Outline platelets.
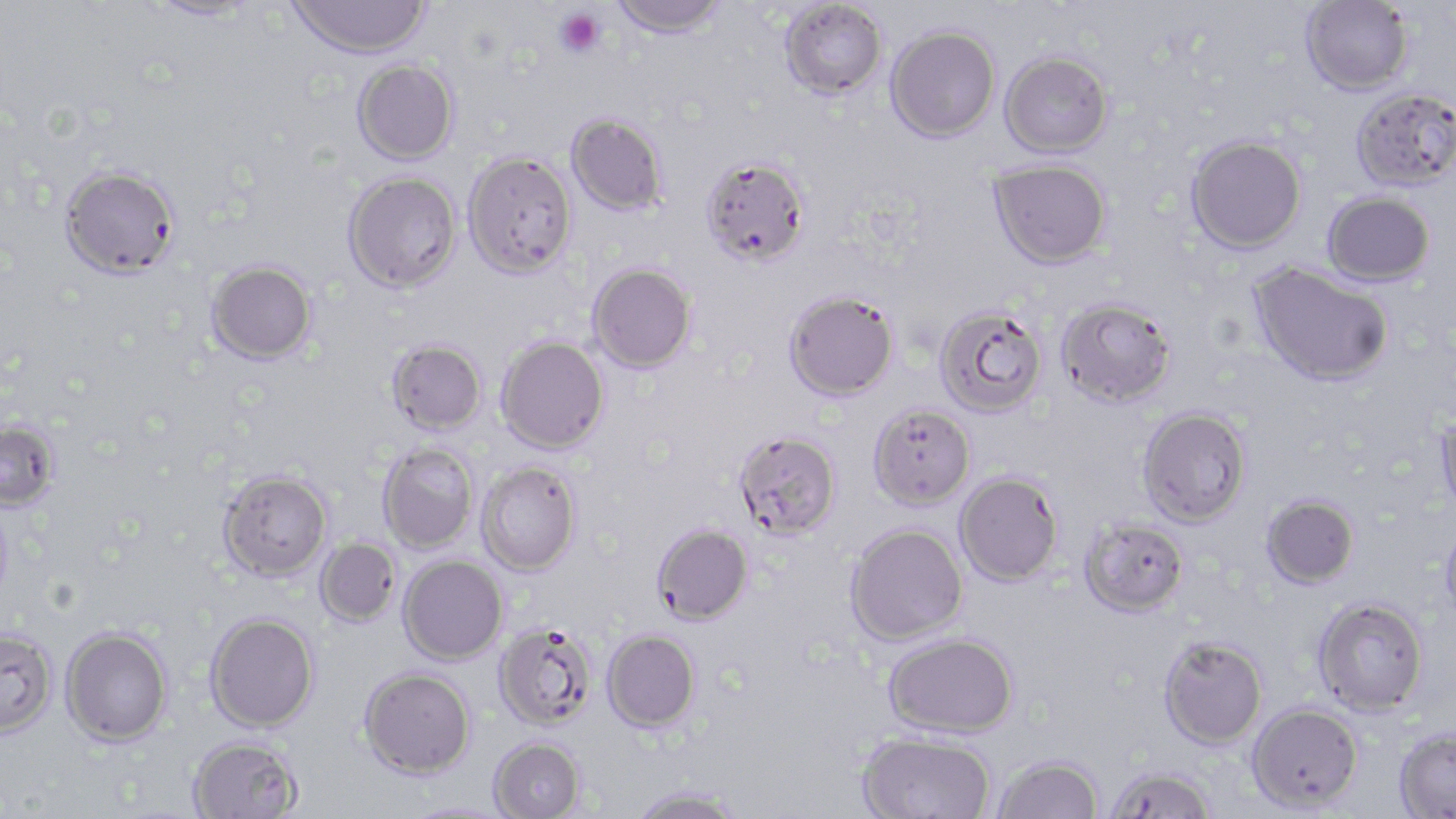

Approximate bounding boxes as [x1, y1, x2, y2] in pixels.
Platelets: [555, 7, 605, 58].

slide-level diagnosis = Plasmodium falciparum
stain = May-Grünwald-Giemsa
uninfected red blood cell locations = approximate bounding boxes as [x1, y1, x2, y2] in pixels: [288, 0, 430, 60], [608, 0, 730, 38], [779, 0, 887, 100], [1300, 0, 1413, 96], [147, 1, 259, 22], [886, 26, 1000, 143], [1000, 51, 1113, 158], [352, 60, 459, 165], [1350, 87, 1456, 193], [566, 113, 668, 217], [1185, 134, 1306, 253], [463, 150, 577, 278], [699, 156, 809, 266], [989, 159, 1111, 268], [60, 165, 180, 277], [343, 171, 461, 293], [1323, 191, 1435, 287], [206, 260, 318, 364], [587, 263, 697, 373], [1249, 264, 1394, 387], [783, 289, 899, 401], [1056, 297, 1176, 407], [934, 305, 1048, 418], [495, 336, 609, 453], [387, 339, 486, 435], [868, 403, 975, 510], [1138, 407, 1251, 527], [1434, 408, 1456, 521], [0, 421, 59, 510], [731, 429, 842, 540], [378, 443, 479, 553], [477, 461, 582, 576], [218, 469, 331, 581], [954, 471, 1064, 586], [1260, 493, 1359, 589], [0, 498, 13, 612], [1079, 517, 1189, 617], [1439, 519, 1456, 627], [652, 522, 754, 624], [845, 523, 968, 645], [316, 539, 400, 626], [399, 555, 507, 665], [1312, 597, 1429, 715], [205, 612, 319, 732], [493, 621, 599, 731], [61, 627, 172, 745], [0, 629, 57, 737], [602, 629, 701, 732], [883, 632, 1018, 738], [1158, 636, 1268, 750], [359, 667, 475, 778], [1247, 703, 1363, 812], [1394, 728, 1456, 818], [856, 730, 995, 819], [188, 736, 304, 819], [488, 737, 585, 819], [992, 754, 1104, 818], [1106, 766, 1214, 818], [628, 786, 744, 819], [402, 801, 513, 819]
image size = 1456×819 pixels
preparation = thin blood film
field of view = one of a larger specimen
magnification = 1000x
modality = light microscopy